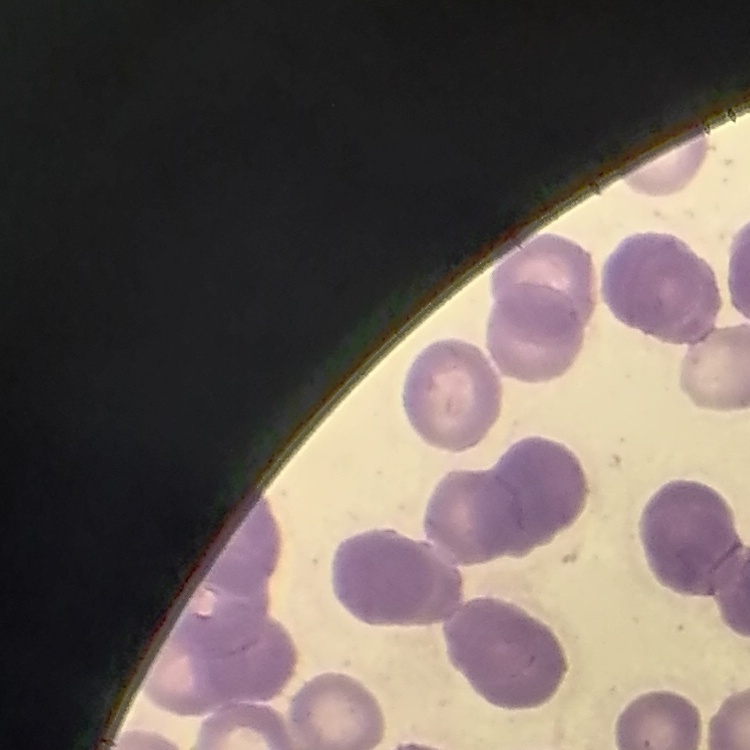
red blood cell morphology = rouleaux formation
image type = square crop of a larger photomicrograph
stain = Field's or Giemsa
preparation = thin blood film